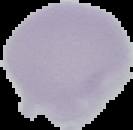
image type = segmented cell region on a black background
image size = 133×130 pixels
preparation = thin blood film
result = negative for malaria parasites